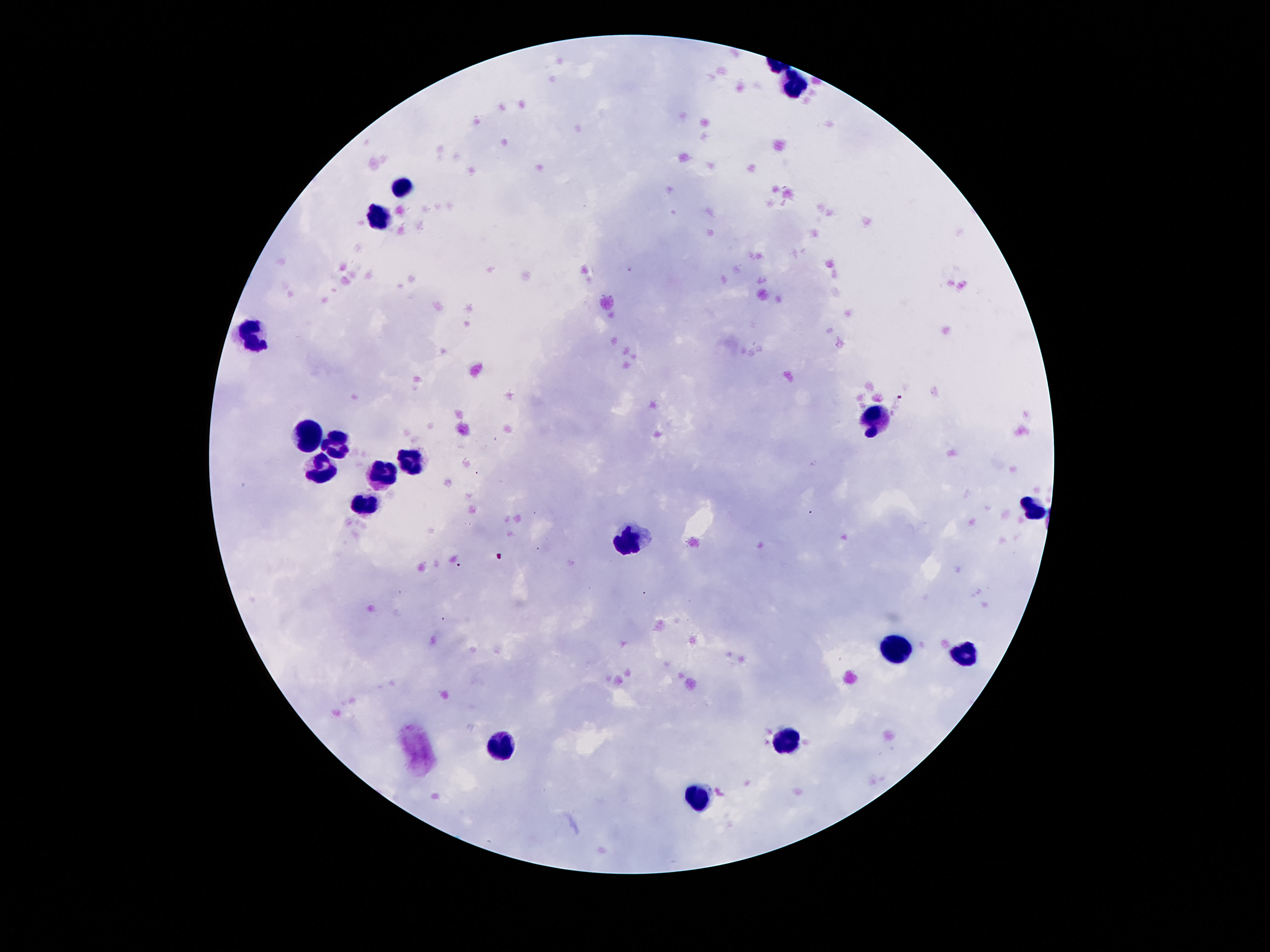

magnification = 100x
field of view = single
capture = smartphone camera through the microscope eyepiece
patient malaria status = not infected
stain = Giemsa
leukocyte locations = approximate centers as (x, y) in pixels: (793, 85), (402, 188), (379, 218), (253, 337), (872, 419), (309, 433), (335, 442), (408, 461), (322, 467), (383, 475), (364, 503), (1030, 509), (627, 542), (891, 651), (963, 656), (501, 745), (786, 745), (700, 801)
preparation = thick blood film
image size = 1270×952 pixels